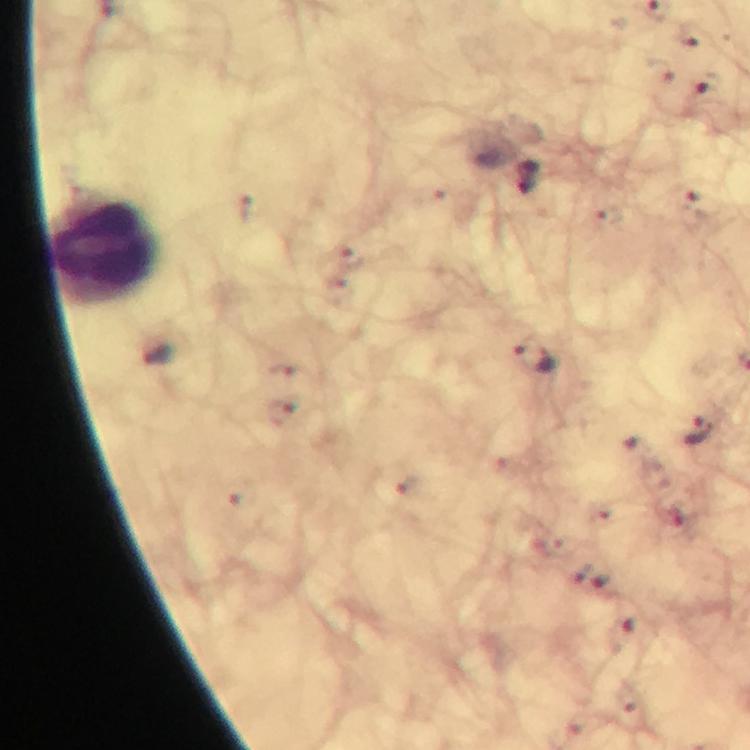

magnification = 100x
cropped from = one field of view
immersion oil = used
capture = smartphone camera through the microscope
leukocyte locations = approximate centers as (x, y) in pixels: (105, 247)
image size = 750×750 pixels
stain = Giemsa
preparation = thick smear
malaria parasite locations = approximate centers as (x, y) in pixels: (690, 35), (708, 86), (533, 177), (693, 208), (348, 254), (339, 291), (159, 358), (534, 358), (288, 371), (281, 412), (701, 433), (639, 448), (408, 484), (242, 502), (670, 515), (579, 570), (600, 586), (624, 634), (629, 700)
context = from a diagnostic examination for malaria